Report the malaria status of this cell.
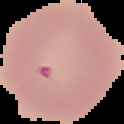
It is parasitized.

preparation: thin blood smear
image_size: 124×124 pixels
image_type: segmented cell region with the area outside set to black